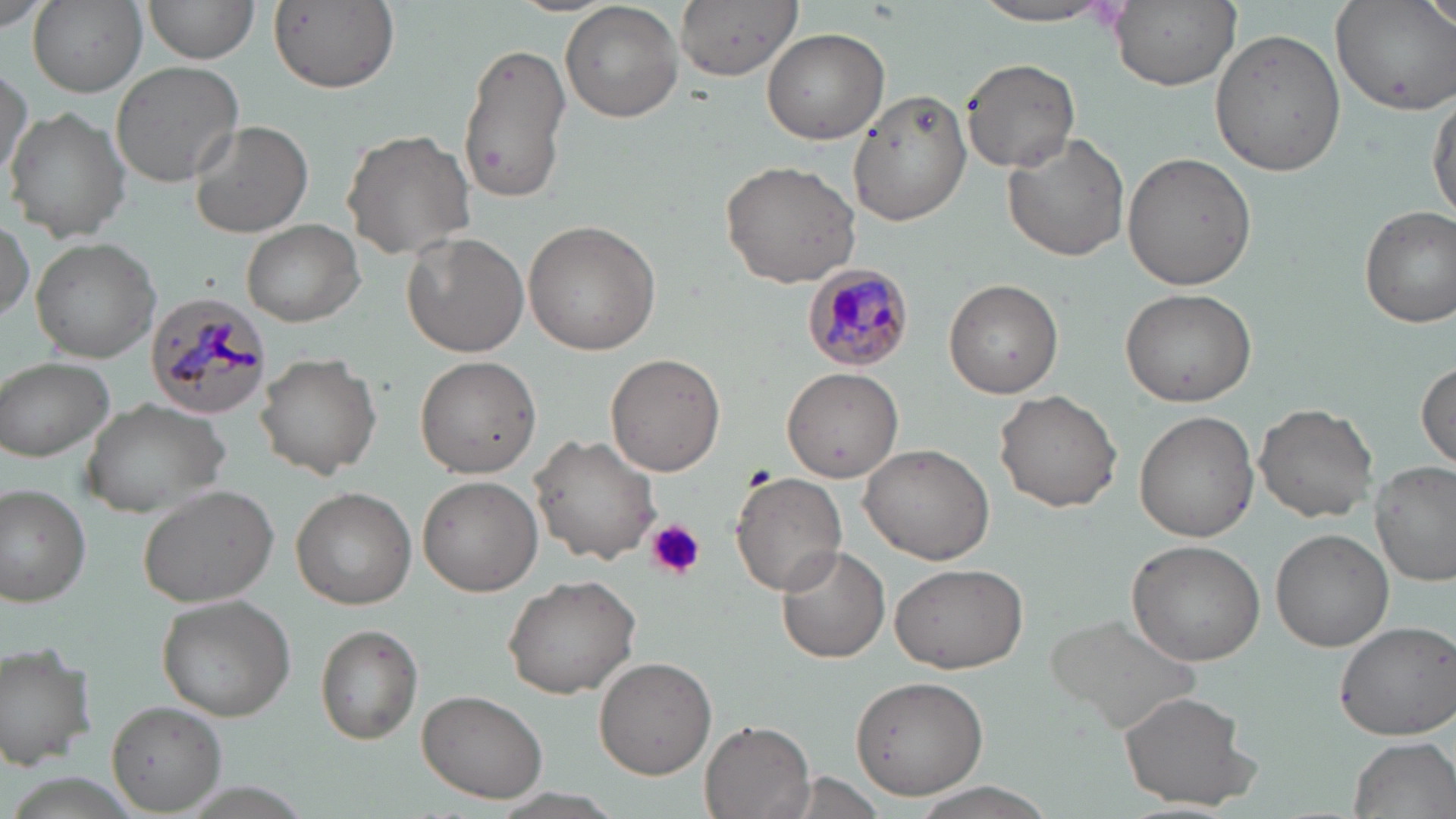

Approximate bounding boxes as (x1, y1, x2, y2) in pixels. Uninfected red blood cell locations: (28, 0, 147, 96), (144, 0, 258, 64), (674, 0, 800, 80), (1109, 0, 1239, 89), (1330, 0, 1456, 115), (1421, 0, 1456, 38), (560, 1, 685, 122), (269, 2, 400, 94), (965, 2, 1122, 26), (0, 4, 58, 36), (1211, 27, 1347, 177), (763, 28, 889, 144), (458, 39, 572, 205), (961, 58, 1079, 172), (109, 61, 245, 189), (0, 64, 32, 187), (847, 90, 973, 226), (1428, 91, 1456, 224), (5, 107, 130, 243), (188, 120, 313, 239), (341, 129, 479, 260), (1004, 135, 1130, 262), (1123, 152, 1256, 292), (720, 158, 863, 288), (1359, 204, 1456, 328), (0, 213, 35, 328), (524, 219, 662, 355), (242, 221, 364, 325), (400, 231, 529, 358), (31, 239, 159, 361), (945, 279, 1063, 398), (1120, 287, 1257, 406), (255, 352, 381, 480), (605, 354, 726, 476), (1, 357, 117, 462), (414, 357, 542, 477), (1415, 362, 1455, 469), (782, 364, 906, 481), (994, 390, 1123, 512), (80, 395, 230, 516), (1254, 402, 1377, 521), (1133, 411, 1258, 542), (530, 434, 661, 565), (860, 443, 994, 565), (1370, 461, 1456, 587), (730, 470, 847, 595), (417, 475, 543, 597), (0, 484, 94, 607), (136, 484, 281, 607), (291, 488, 417, 609), (1272, 529, 1393, 651), (1127, 538, 1267, 665), (775, 544, 891, 664), (891, 562, 1028, 674), (503, 572, 644, 698), (157, 592, 296, 720), (1043, 612, 1203, 735), (1332, 618, 1456, 741), (314, 625, 424, 743), (0, 642, 98, 770), (594, 655, 718, 779), (848, 673, 989, 800), (417, 689, 548, 804), (1118, 690, 1258, 809), (108, 701, 226, 813), (700, 717, 815, 819), (1346, 735, 1455, 818), (490, 790, 628, 819). Platelet locations: (647, 519, 704, 579). Plasmodium malariae-infected red blood cell locations: (803, 264, 916, 368), (145, 291, 271, 419). Slide-level diagnosis: Plasmodium malariae. Captured at 1000x magnification. Light microscopy. Thin blood film. Single field of view. Image is 1456×819 pixels. May-Grünwald-Giemsa stain.